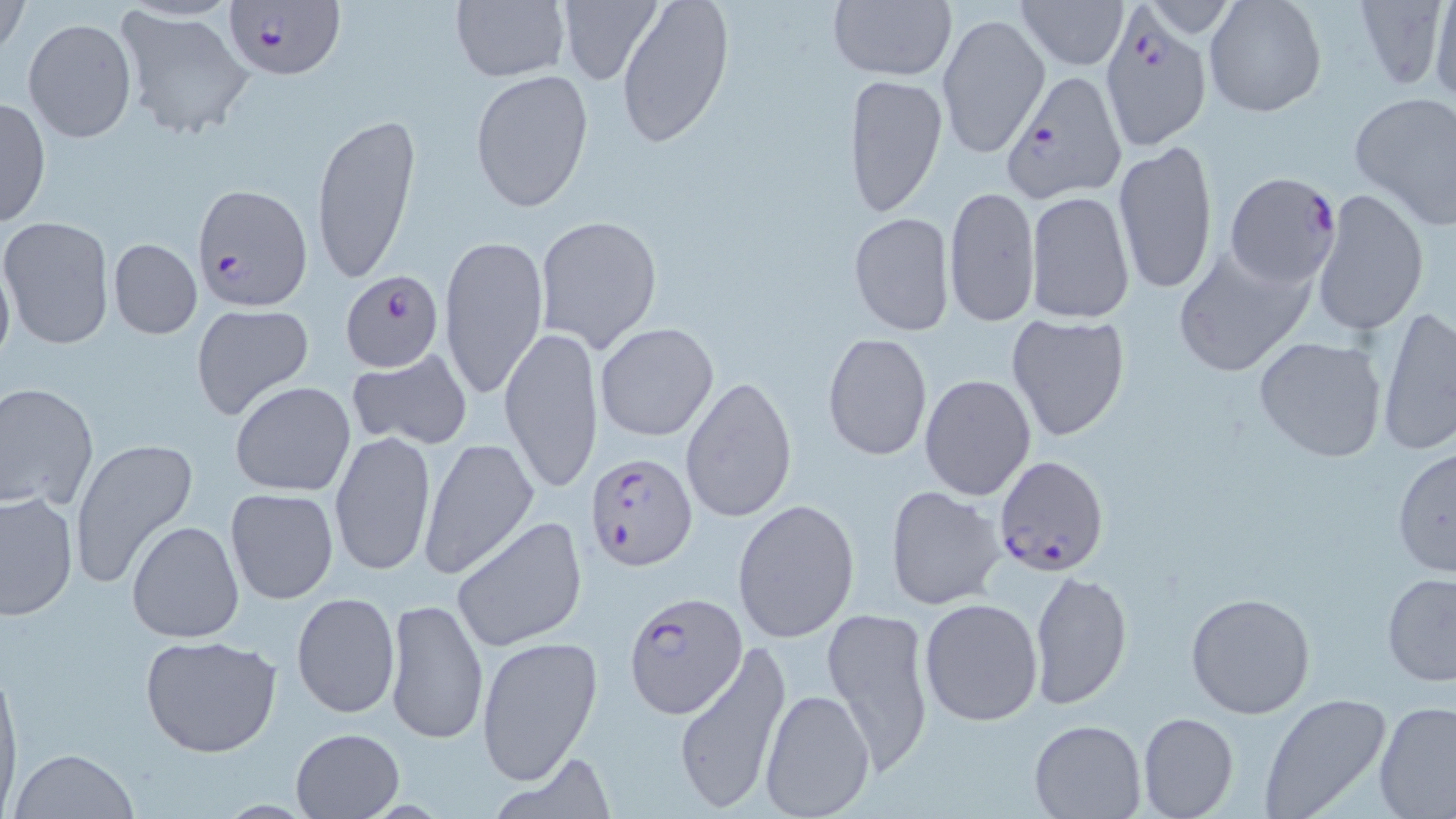
Approximate bounding boxes as (x1, y1, x2, y2) in pixels. Plasmodium falciparum-infected red blood cell locations: (223, 0, 344, 82), (1100, 11, 1212, 149), (1002, 69, 1126, 204), (1225, 171, 1341, 288), (191, 183, 314, 311), (340, 272, 443, 369), (587, 452, 697, 572), (994, 455, 1108, 577), (623, 590, 743, 719). Uninfected red blood cell locations: (0, 0, 29, 59), (450, 0, 569, 83), (617, 0, 734, 149), (1014, 0, 1127, 69), (1204, 0, 1327, 120), (1351, 0, 1451, 94), (827, 1, 957, 81), (1423, 1, 1456, 105), (555, 2, 664, 87), (116, 8, 255, 141), (937, 12, 1047, 159), (23, 18, 137, 144), (470, 69, 596, 214), (843, 72, 947, 218), (1348, 92, 1456, 228), (1, 98, 51, 230), (310, 111, 422, 289), (1112, 138, 1220, 298), (944, 184, 1040, 327), (1313, 189, 1430, 337), (1026, 190, 1135, 323), (849, 212, 953, 334), (535, 215, 662, 354), (1, 218, 114, 350), (439, 234, 549, 400), (108, 238, 202, 339), (1172, 244, 1316, 378), (0, 248, 15, 375), (190, 304, 316, 422), (1376, 308, 1456, 454), (1006, 313, 1131, 441), (596, 321, 718, 442), (500, 326, 603, 494), (621, 329, 773, 476), (822, 332, 932, 461), (1252, 335, 1388, 462), (347, 348, 472, 451), (919, 373, 1036, 502), (680, 375, 796, 523), (230, 381, 356, 498), (0, 382, 99, 510), (329, 431, 437, 577), (419, 436, 541, 579), (69, 437, 196, 589), (1392, 446, 1455, 577), (884, 484, 1007, 611), (225, 486, 340, 605), (0, 490, 77, 621), (732, 498, 861, 642), (450, 516, 588, 652), (126, 519, 244, 643), (1028, 570, 1132, 708), (1380, 574, 1456, 687), (1186, 591, 1315, 720), (291, 592, 400, 719), (383, 596, 488, 747), (918, 596, 1044, 727), (823, 606, 936, 780), (139, 633, 283, 758), (475, 635, 602, 786), (672, 638, 793, 812), (0, 657, 21, 807), (759, 687, 876, 818), (1258, 692, 1394, 819), (1374, 701, 1456, 818), (1138, 712, 1238, 819), (1028, 719, 1146, 818), (291, 728, 404, 818), (8, 748, 140, 819), (486, 751, 619, 819). Slide-level diagnosis: Plasmodium falciparum. Light microscopy. Captured at 1000x magnification. Single field of view. Thin blood smear. May-Grünwald-Giemsa-stained preparation. Image is 1456×819 pixels.